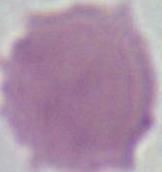

magnification: 1000x
identification: red blood cell
modality: photomicrograph